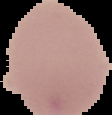
Malaria status: uninfected. Image is 112×115 pixels. From a thin blood film. Cell region segmented out of the field of view; the surrounding area is masked to black.